Identify the parasite.
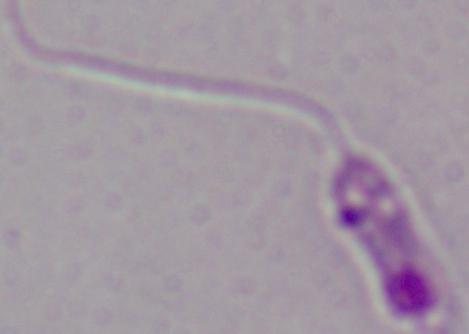

This is Leishmania.

Photomicrograph. 1000x magnification.